Classify this cell by malaria status.
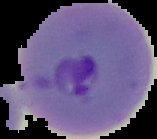

Parasitized.

{
  "image_size": "157×139 pixels",
  "preparation": "thin blood film",
  "image_type": "segmented cell region with the area outside set to black"
}